Report the malaria status of this cell.
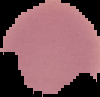
Uninfected.

From a thin blood film. Image is 100×97 pixels. Cell region segmented out of the field of view; the surrounding area is masked to black.